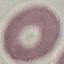
Summary:
  - Result: no malaria parasites seen
  - Image type: automatically extracted cell patch, resized to 64 × 64 pixels
  - Preparation: thin smear
  - Stain: Giemsa
  - Capture: smartphone camera at the microscope eyepiece